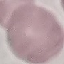

Summary:
  - Result: no malaria parasites detected
  - Capture: smartphone through the microscope eyepiece
  - Image type: automatically extracted cell patch, resized to 64 × 64 pixels
  - Preparation: thin blood smear
  - Stain: Giemsa